State the blood parasite species.
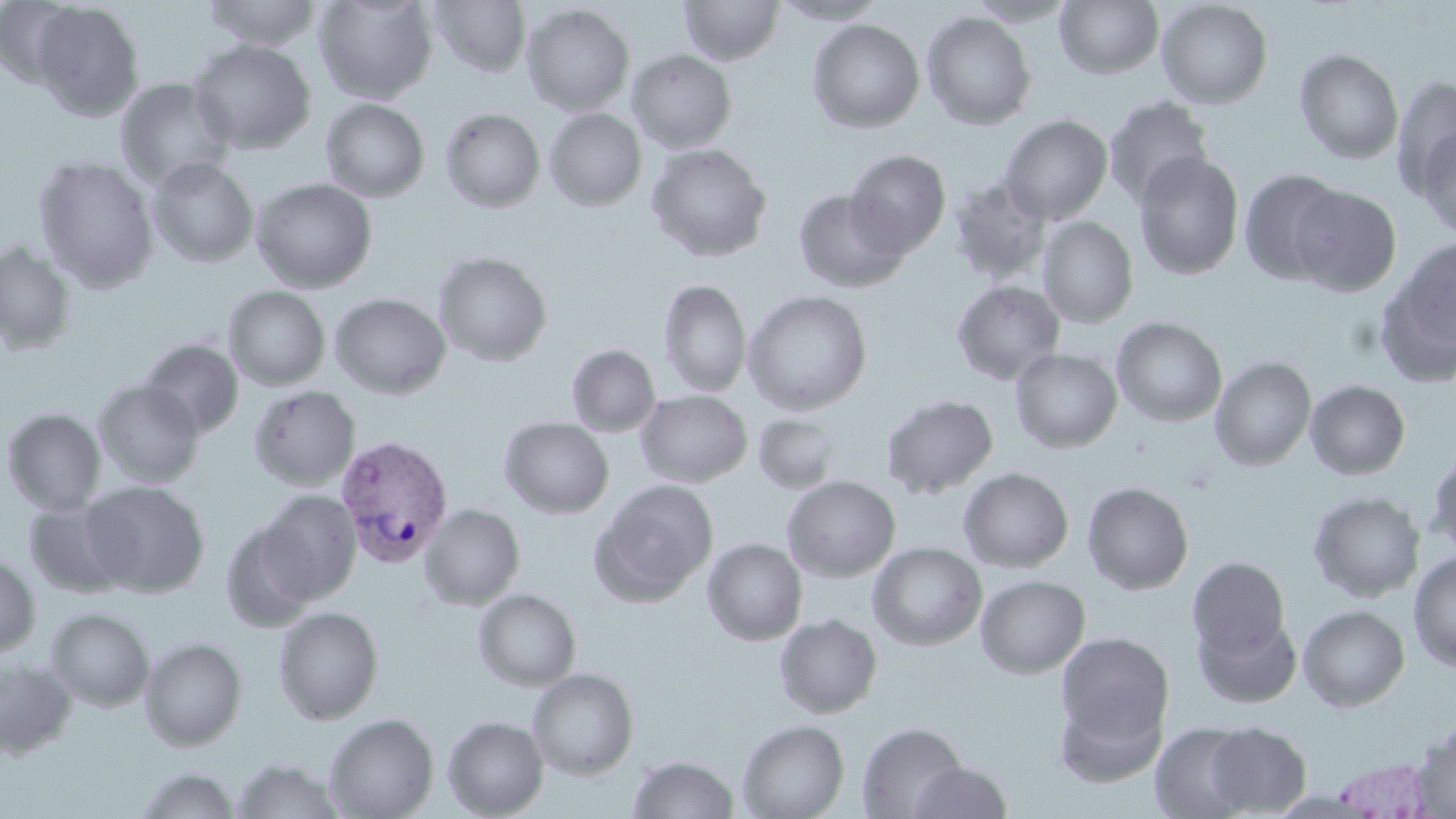

Plasmodium vivax.

Approximate bounding boxes as (x1,y1)-(x2,y2) corner pairs in pixels. Uninfected red blood cell locations: (0,0)-(82,87), (200,0)-(324,50), (314,0)-(437,104), (427,0)-(531,78), (679,0)-(784,65), (772,0)-(888,25), (965,0)-(1078,26), (1156,0)-(1273,110), (1055,1)-(1164,79), (32,2)-(145,121), (522,4)-(635,116), (921,11)-(1036,130), (807,19)-(925,133), (188,39)-(316,155), (1294,48)-(1404,164), (627,49)-(737,154), (636,50)-(758,247), (1391,76)-(1456,197), (115,77)-(235,190), (1103,95)-(1215,209), (320,98)-(430,202), (440,108)-(545,213), (544,108)-(647,212), (999,114)-(1113,224), (1415,125)-(1456,241), (646,143)-(772,263), (845,149)-(951,258), (1133,151)-(1245,280), (34,156)-(159,292), (147,157)-(259,268), (1238,168)-(1346,284), (949,177)-(1053,285), (250,178)-(377,293), (1288,185)-(1401,296), (792,189)-(910,293), (1037,217)-(1138,328), (1378,238)-(1456,380), (0,242)-(77,355), (433,251)-(553,367), (658,280)-(752,397), (951,280)-(1065,385), (223,286)-(330,391), (743,290)-(873,415), (329,293)-(451,399), (1112,317)-(1227,427), (139,339)-(244,437), (566,344)-(661,437), (1010,349)-(1123,453), (1209,356)-(1316,470), (93,380)-(205,488), (1305,380)-(1411,480), (248,385)-(361,490), (635,390)-(752,487), (880,394)-(999,499), (2,408)-(107,515), (752,414)-(841,494), (499,417)-(614,519), (1426,444)-(1456,561), (958,467)-(1074,573), (782,476)-(901,582), (591,479)-(719,605), (81,481)-(210,597), (1082,481)-(1194,595), (256,490)-(361,604), (1308,491)-(1426,602), (23,499)-(132,599), (419,504)-(525,610), (220,519)-(321,632), (702,538)-(807,646), (867,542)-(987,651), (1408,552)-(1456,671), (0,554)-(40,657), (1187,556)-(1291,660), (975,575)-(1090,678), (473,589)-(582,691), (1298,605)-(1410,711), (274,606)-(384,725), (46,608)-(154,711), (774,614)-(883,718), (1195,614)-(1302,708), (1056,633)-(1175,747), (140,637)-(247,751), (0,658)-(77,760), (527,668)-(639,780), (1055,692)-(1167,787), (324,713)-(439,819), (443,716)-(548,818), (738,718)-(850,819), (856,721)-(968,818), (1150,722)-(1254,819), (1205,722)-(1311,816), (1411,724)-(1456,816), (629,754)-(738,818), (1331,758)-(1436,818), (232,759)-(343,819), (907,761)-(1013,818), (135,767)-(240,818). Plasmodium vivax-infected red blood cell locations: (333,435)-(451,568). Thin blood smear. Image is 1456×819 pixels. 1000x magnification. Optical microscopy. May-Grünwald-Giemsa stain. One field of a larger specimen.